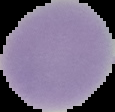 From a thin blood smear. Image is 115×112 pixels. Segmented cell region on a black background. Malaria status: uninfected.